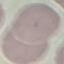

malaria_status: uninfected
stain: Giemsa
image_type: automatically extracted cell patch, resized to 64 × 64 pixels
capture: smartphone through the microscope eyepiece
preparation: thin blood film